Classify this cell by malaria status.
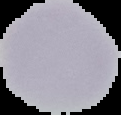
Uninfected.

{
  "image_type": "cell region segmented out of the field of view; surrounding area masked to black",
  "image_size": "121×115 pixels",
  "preparation": "thin blood smear"
}